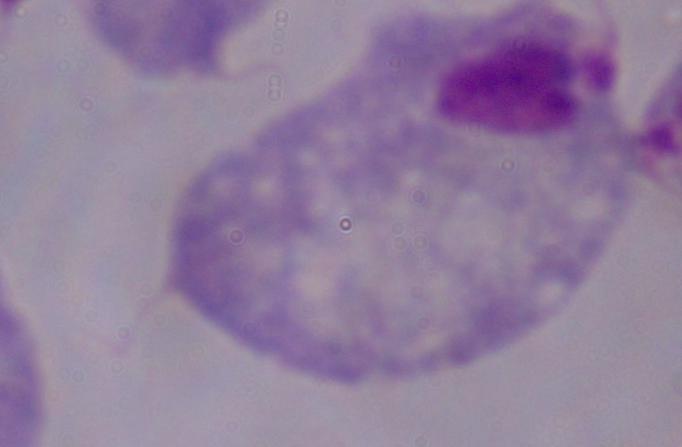
Photomicrograph. 1000x magnification. A trichomonad is seen.